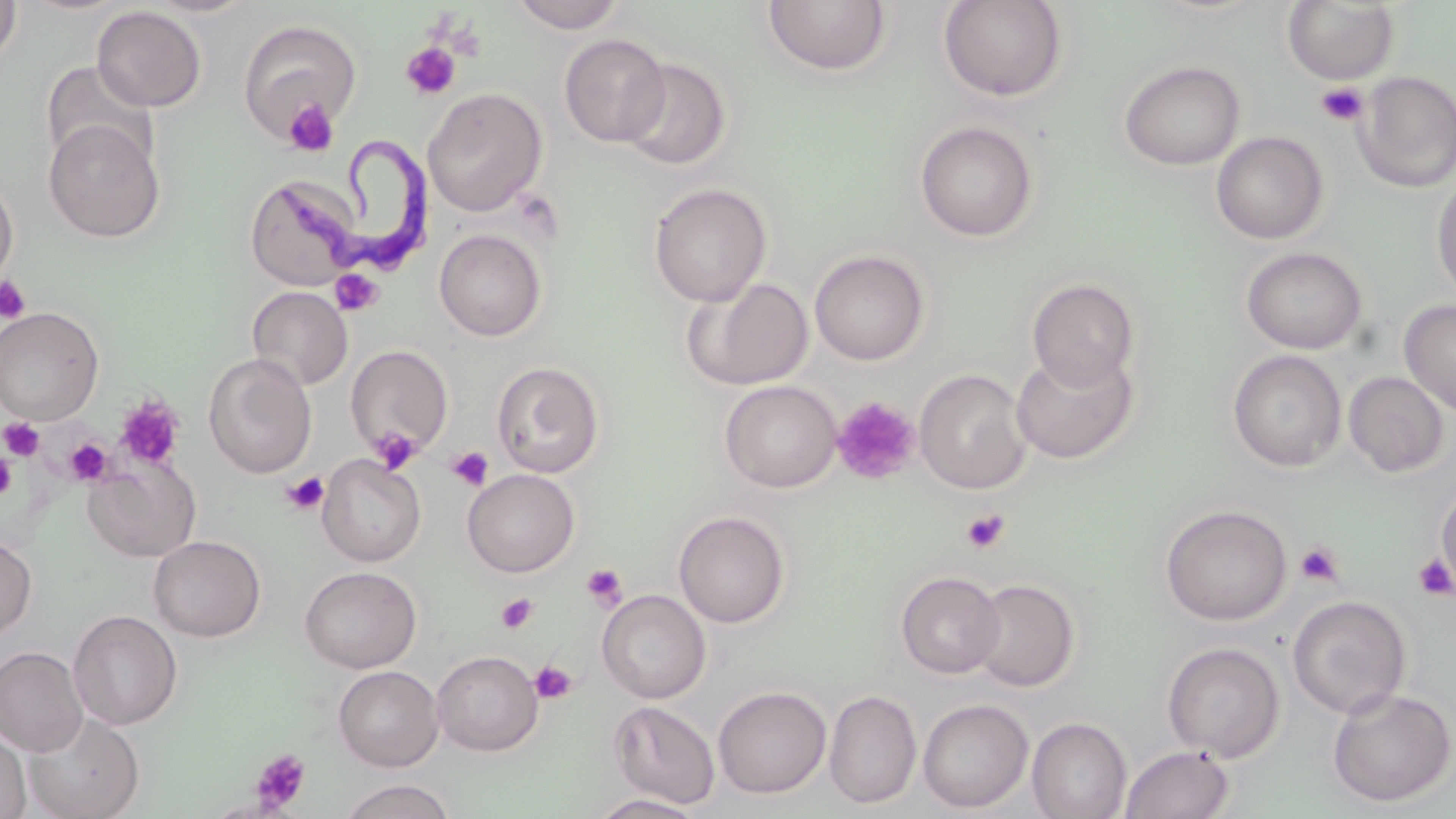
{
  "slide_level_diagnosis": "Trypanosoma brucei",
  "magnification": "1000x",
  "trypanosoma_brucei_locations": "approximate bounding boxes as (x1,y1)-(x2,y2) corner pairs in pixels: (279,129)-(437,294)",
  "image_size": "1456×819 pixels",
  "preparation": "thin blood smear",
  "stain": "May-Grünwald-Giemsa",
  "field_of_view": "single",
  "uninfected_red_blood_cell_locations": "approximate bounding boxes as (x1,y1)-(x2,y2) corner pairs in pixels: (0,0)-(22,67), (144,0)-(259,18), (509,0)-(627,33), (763,0)-(891,78), (938,0)-(1069,102), (1282,1)-(1399,85), (91,6)-(207,112), (237,19)-(363,141), (559,33)-(671,147), (620,58)-(731,171), (41,60)-(157,170), (1119,60)-(1245,170), (1355,71)-(1456,193), (423,88)-(547,217), (44,118)-(165,243), (914,120)-(1039,242), (1211,131)-(1329,244), (0,173)-(18,290), (245,175)-(361,291), (1431,176)-(1456,304), (648,183)-(772,307), (434,229)-(546,341), (1241,246)-(1368,355), (809,249)-(929,365), (685,277)-(813,391), (1027,278)-(1141,392), (246,286)-(353,391), (1398,299)-(1456,417), (0,306)-(104,424), (345,345)-(453,458), (1011,350)-(1138,465), (1227,350)-(1347,472), (203,353)-(317,478), (491,360)-(605,478), (914,369)-(1032,494), (1343,371)-(1450,477), (719,380)-(842,492), (317,454)-(426,567), (82,455)-(201,562), (462,469)-(580,577), (1436,483)-(1456,594), (1159,503)-(1293,626), (673,510)-(791,628), (0,535)-(37,641), (149,536)-(265,642), (299,566)-(421,673), (895,570)-(1006,678), (968,577)-(1080,692), (597,590)-(711,703), (1287,595)-(1412,718), (68,609)-(182,731), (1161,642)-(1285,762), (0,646)-(88,757), (431,650)-(543,756), (334,665)-(443,772), (713,686)-(832,799), (1326,687)-(1455,808), (823,689)-(922,809), (918,698)-(1034,813), (608,700)-(720,810), (23,710)-(145,819), (1027,717)-(1132,819), (0,727)-(31,819), (1120,744)-(1234,819), (337,779)-(457,819), (588,793)-(708,818)",
  "platelet_locations": "approximate bounding boxes as (x1,y1)-(x2,y2) corner pairs in pixels: (400,42)-(461,101), (1317,82)-(1369,126), (282,97)-(339,156), (330,269)-(383,316), (0,275)-(31,324), (831,395)-(922,485), (114,396)-(184,471), (1,418)-(45,461), (372,426)-(421,474), (65,437)-(114,486), (447,446)-(494,491), (0,452)-(16,501), (281,471)-(329,515), (961,509)-(1010,553), (1295,541)-(1345,587), (1413,554)-(1455,602), (581,563)-(626,610), (496,594)-(538,635), (530,660)-(577,705), (250,749)-(312,813)",
  "modality": "light microscopy"
}